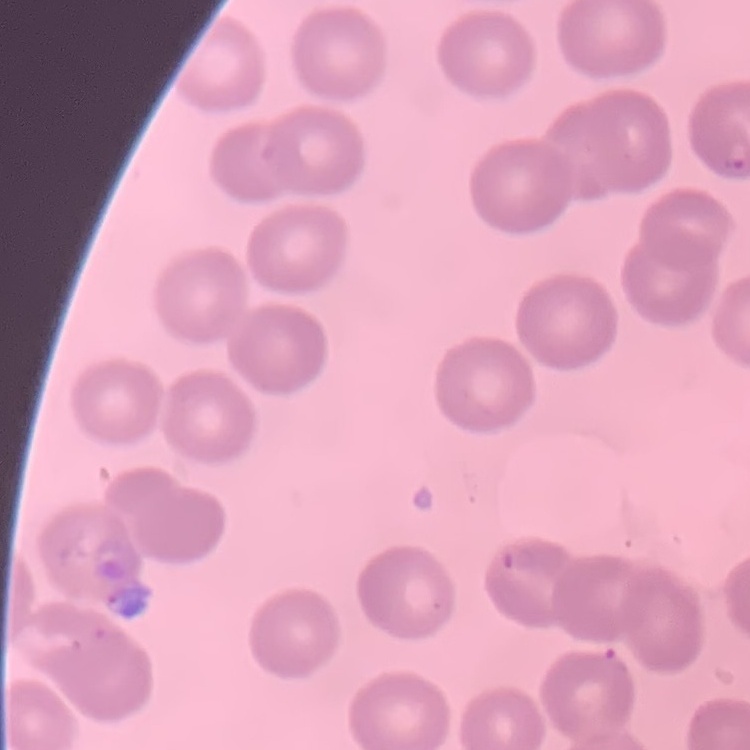
Summary:
  - Red blood cell morphology: no rouleaux formation
  - Preparation: thin peripheral smear
  - Image type: one tile cut from a larger photomicrograph
  - Stain: Field's or Giemsa